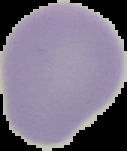

Summary:
  - Malaria status: uninfected
  - Image size: 127×151 pixels
  - Preparation: thin blood film
  - Image type: segmented cell region with the area outside set to black